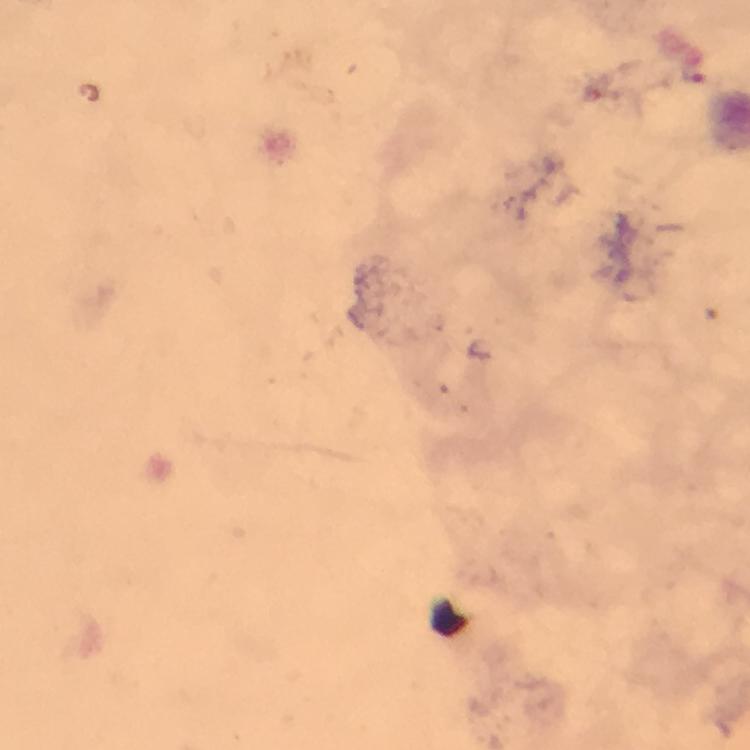

Approximate centers as [x, y] in pixels.
Summary:
  - Plasmodium parasite locations: [692, 71]
  - Capture: smartphone camera through the microscope
  - Immersion oil: applied
  - Preparation: thick smear
  - Cropped from: a single field of view
  - Context: from a diagnostic examination for malaria
  - Stain: Giemsa
  - Magnification: 100x
  - Image size: 750×750 pixels